Evaluate for malaria.
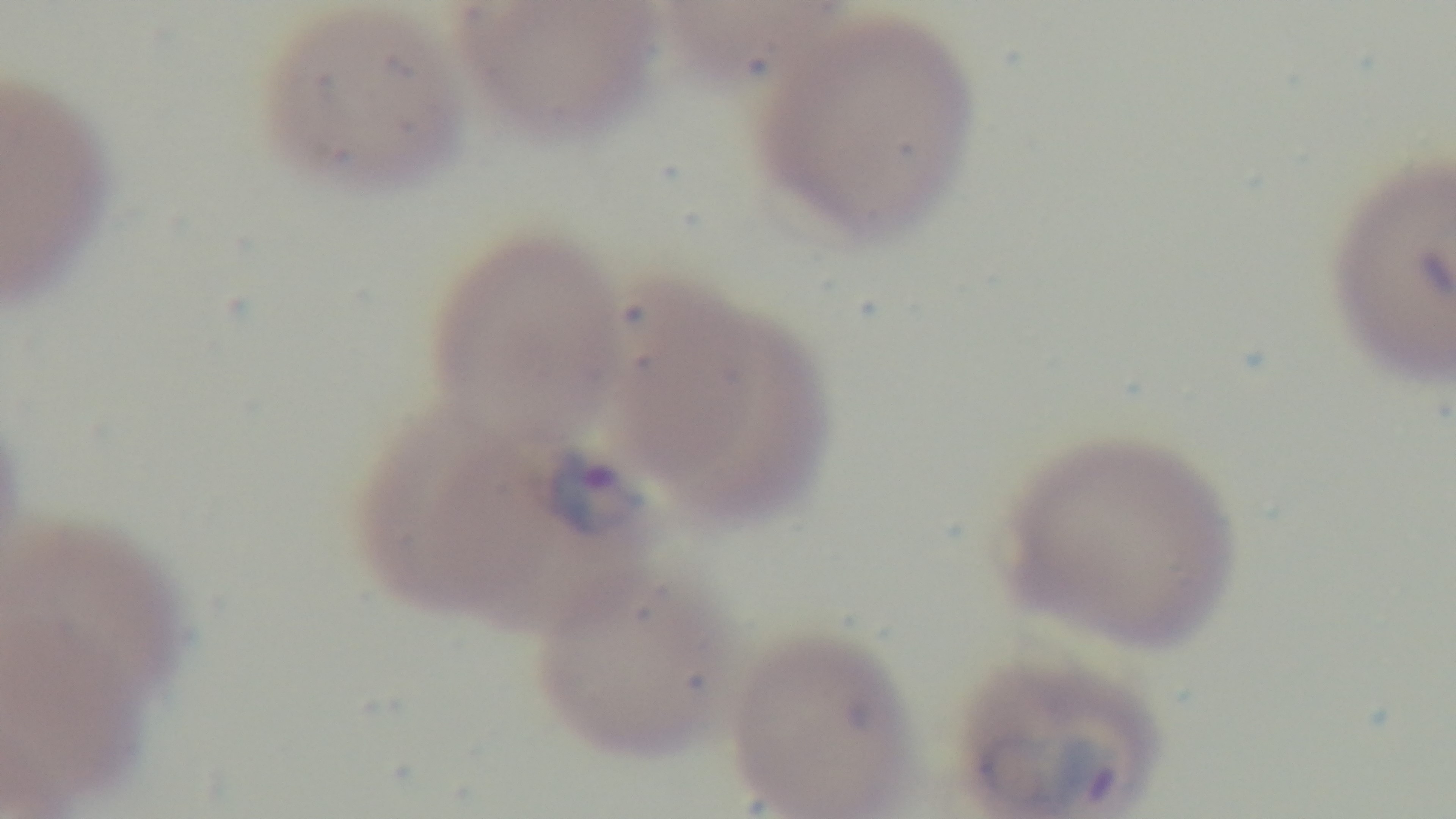

It is infected.

Light microscopy. One field from the slide. Oil-immersion objective, 100x. Preparation: thin blood film. Captured with a mounted 4K digital camera. Giemsa-stained.